Locate every leukocyte (white blood cell).
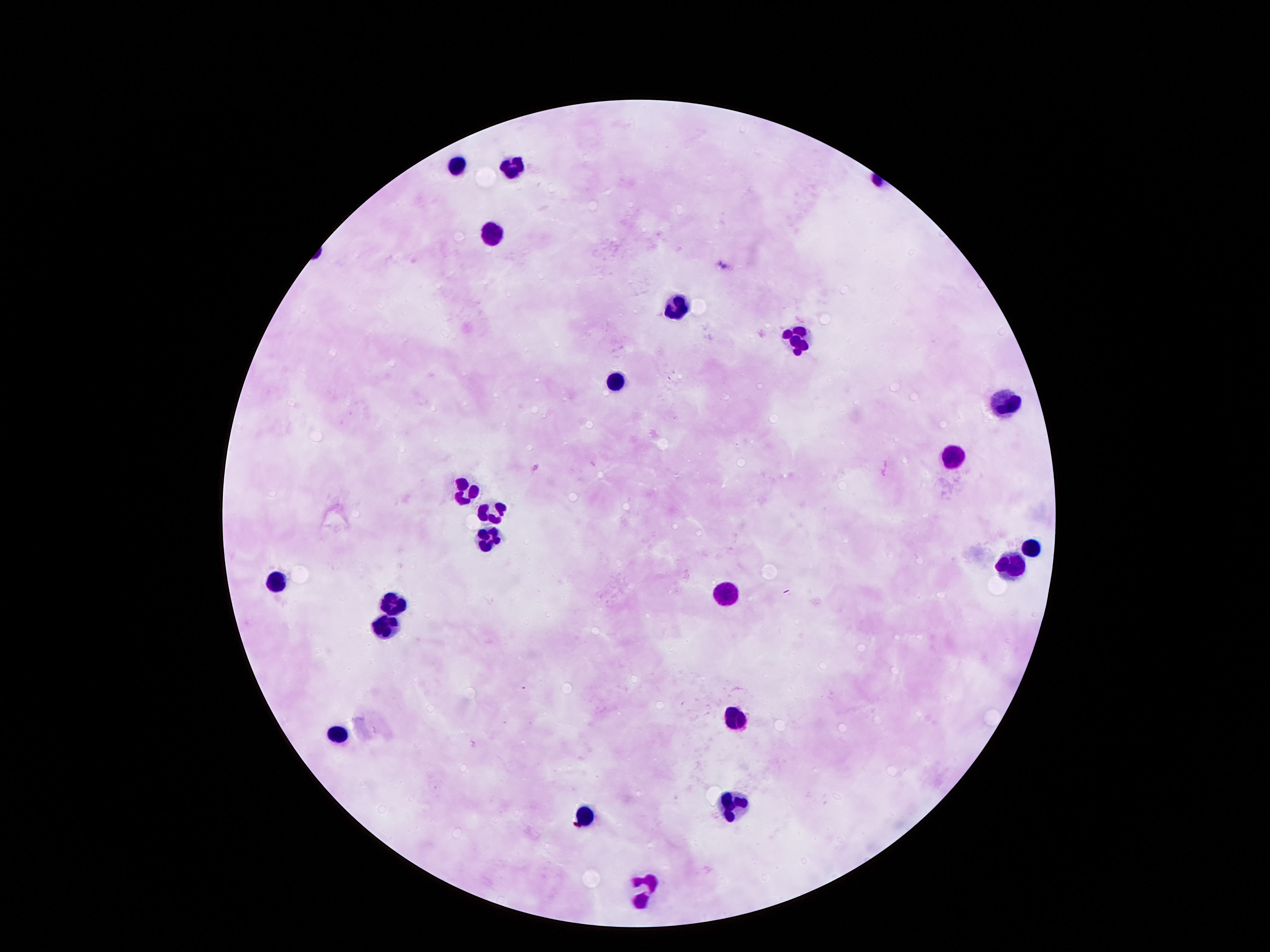

Approximate centers as [x, y] in pixels.
Leukocytes: [461, 164], [511, 164], [491, 231], [675, 309], [792, 338], [616, 381], [1011, 398], [953, 453], [464, 489], [490, 510], [485, 538], [1031, 543], [1012, 568], [276, 581], [728, 588], [391, 606], [384, 622], [733, 714], [336, 730], [733, 796], [584, 817], [642, 882].

field of view = one from this slide
capture = smartphone camera through the microscope eyepiece
patient malaria status = not infected
stain = Giemsa
image size = 1270×952 pixels
magnification = 100x
preparation = thick blood film